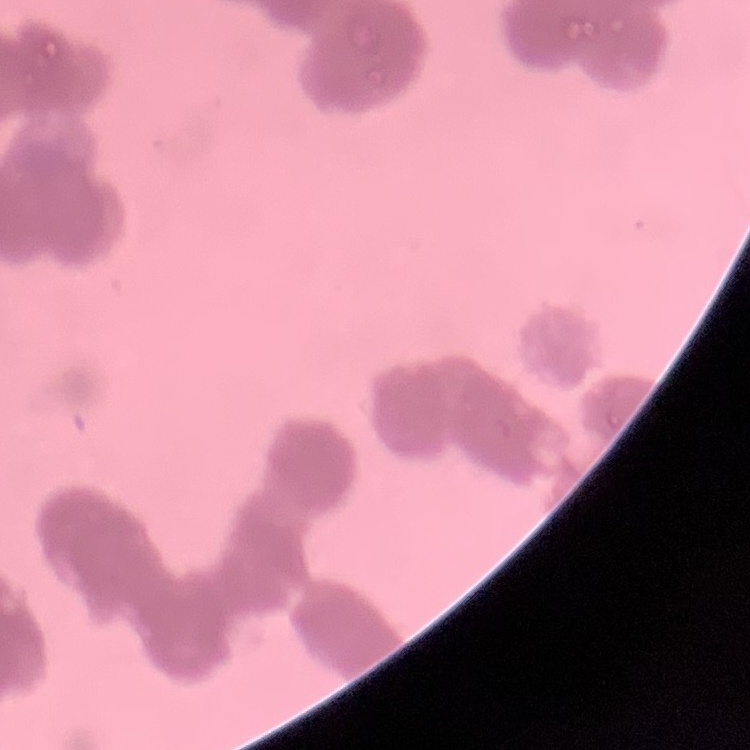

red_blood_cell_morphology: rouleaux formation
image_type: square crop of a larger photomicrograph
preparation: thin blood film
stain: Field's or Giemsa